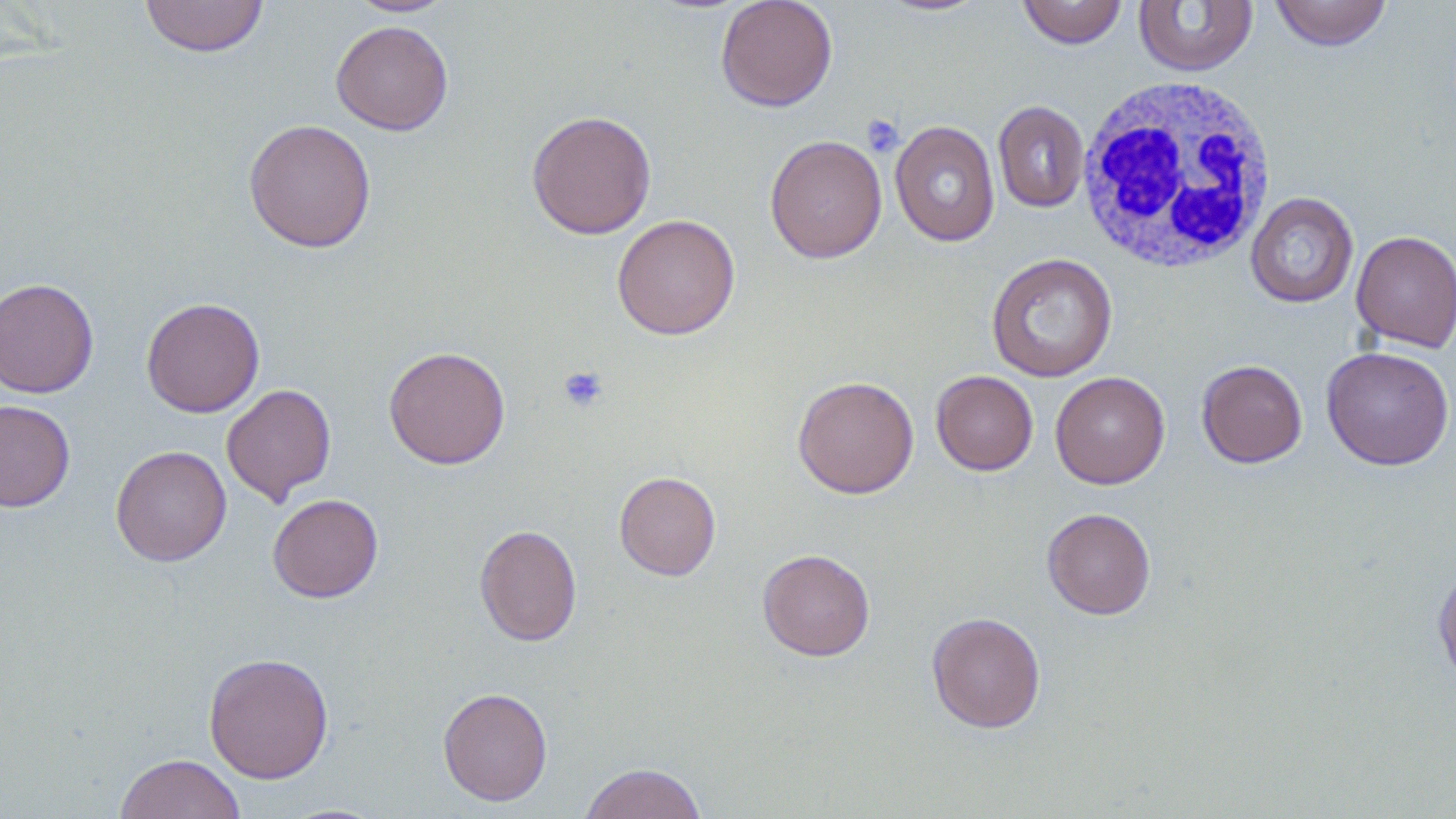
Approximate bounding boxes as [x1, y1, x2, y2] in pixels. White blood cell locations: [1076, 74, 1279, 274]. Platelet locations: [862, 115, 904, 157], [557, 365, 609, 413]. Uninfected red blood cell locations: [139, 0, 269, 58], [715, 0, 838, 112], [873, 0, 994, 17], [1017, 0, 1128, 49], [1269, 0, 1393, 51], [346, 1, 456, 17], [1133, 1, 1259, 77], [331, 20, 454, 135], [993, 101, 1090, 213], [526, 109, 656, 240], [243, 119, 376, 253], [890, 121, 1001, 246], [764, 134, 887, 264], [1245, 192, 1359, 308], [611, 214, 741, 340], [1351, 229, 1455, 352], [985, 252, 1118, 382], [0, 278, 100, 398], [141, 297, 265, 417], [383, 346, 511, 469], [1321, 346, 1454, 470], [1196, 359, 1308, 468], [931, 370, 1038, 476], [1050, 371, 1170, 489], [792, 375, 920, 499], [221, 384, 337, 505], [0, 399, 76, 512], [111, 445, 232, 566], [614, 471, 721, 581], [267, 494, 383, 602], [1041, 507, 1156, 619], [475, 523, 582, 646], [757, 548, 875, 661], [1433, 567, 1456, 689], [926, 611, 1046, 733], [203, 651, 334, 784], [437, 686, 553, 806], [115, 753, 246, 819], [578, 762, 709, 819]. Slide-level diagnosis: no evidence of blood parasites. Light microscopy. Single field of view. Image is 1456×819 pixels. Thin blood film. May-Grünwald-Giemsa-stained preparation. 1000x magnification.